Report the malaria status of this cell.
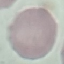

It is uninfected.

Acquired by smartphone through the microscope eyepiece. Automatically extracted cell patch, resized to 64 × 64 pixels. Thin smear of blood. Giemsa stain.